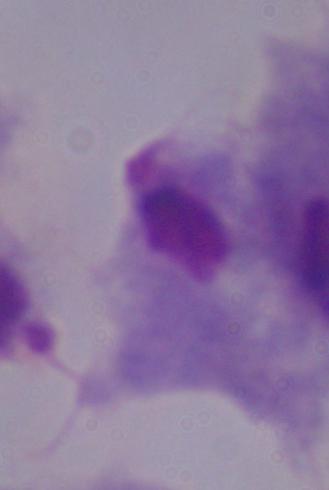
modality = photomicrograph
identification = trichomonad
magnification = 1000x